Assess this cell for malaria.
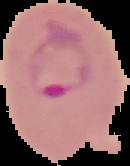

It is parasitized.

Summary:
  - Preparation: thin blood smear
  - Image type: segmented cell region with the area outside set to black
  - Image size: 130×166 pixels